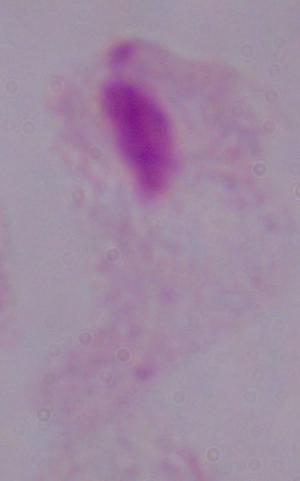 A trichomonad is seen. 1000x magnification. Photomicrograph.